Assess this cell for malaria.
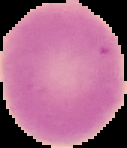
Uninfected.

Image is 127×148 pixels. The area outside the segmented cell region is set to black. From a thin blood film.